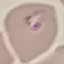

Result: malaria parasites identified. Photographed with a smartphone camera at the microscope eyepiece. Automatically extracted cell patch, resized to 64 × 64 pixels. Thin blood film. Giemsa stain.